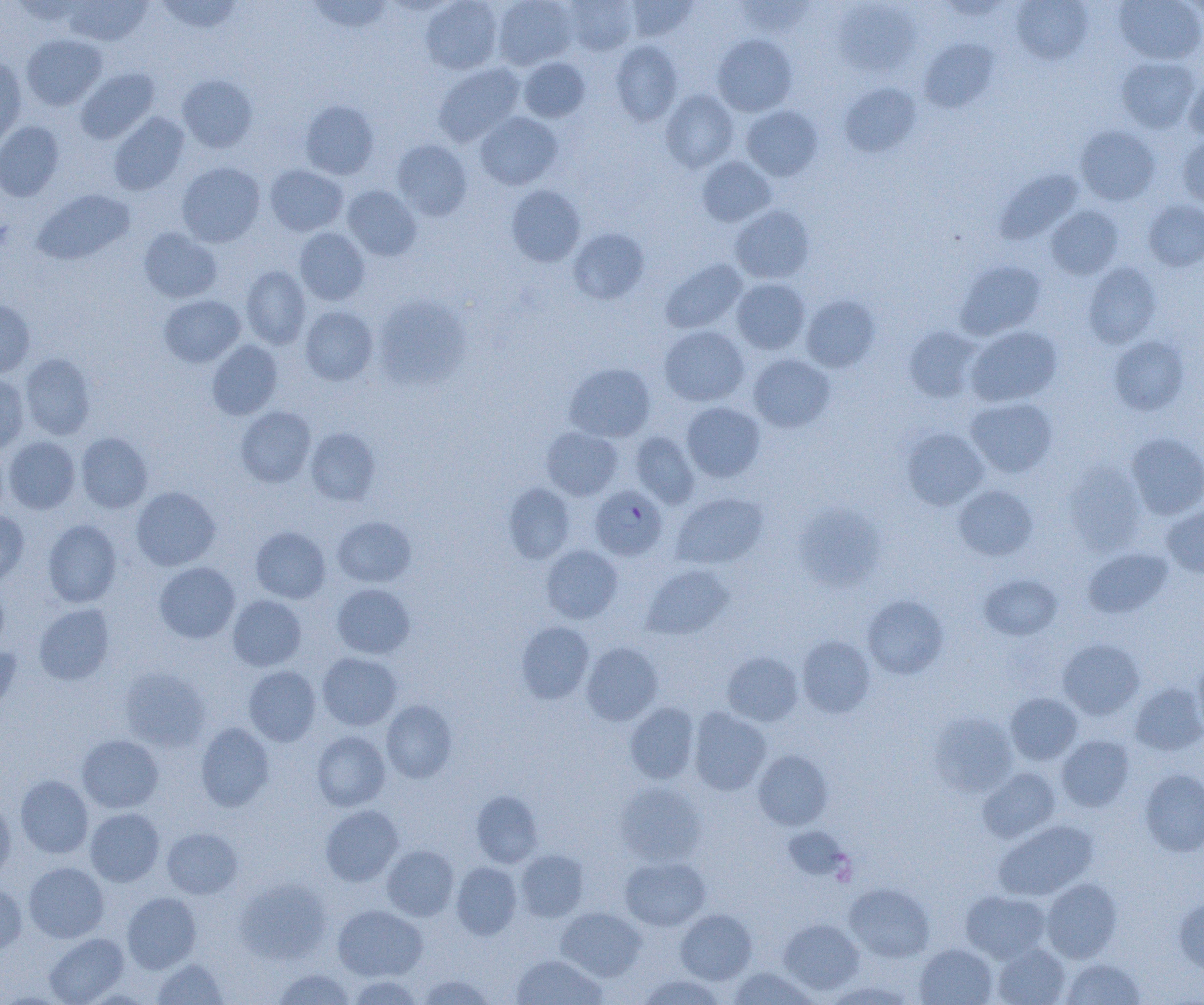
Summary:
  - Coordinate format: approximate bounding boxes as (x1, y1, x2, y2) in pixels
  - Uninfected red blood cell locations: (63, 0, 152, 46), (157, 0, 242, 33), (308, 0, 393, 33), (421, 0, 502, 74), (493, 0, 578, 70), (625, 0, 697, 42), (1011, 0, 1093, 65), (1114, 0, 1204, 64), (566, 1, 637, 55), (735, 1, 816, 36), (835, 2, 920, 76), (21, 34, 107, 110), (712, 35, 797, 117), (920, 39, 998, 112), (610, 40, 683, 125), (0, 55, 26, 149), (518, 57, 590, 122), (1115, 57, 1201, 133), (433, 63, 525, 146), (76, 68, 159, 144), (1184, 72, 1204, 143), (177, 74, 257, 152), (839, 82, 921, 157), (661, 89, 739, 172), (300, 100, 379, 179), (741, 106, 823, 181), (108, 112, 189, 195), (476, 112, 562, 190), (0, 121, 64, 202), (1075, 126, 1160, 205), (1178, 135, 1204, 209), (392, 139, 472, 220), (696, 156, 776, 227), (176, 162, 265, 247), (265, 165, 348, 236), (995, 169, 1084, 244), (343, 185, 422, 260), (506, 185, 585, 267), (33, 189, 135, 265), (1143, 199, 1204, 272), (730, 205, 814, 283), (1046, 206, 1122, 279), (139, 227, 222, 303), (294, 228, 370, 305), (568, 228, 649, 304), (660, 259, 747, 333), (955, 260, 1046, 339), (1083, 262, 1161, 348), (241, 265, 310, 349), (732, 278, 810, 354), (373, 294, 471, 390), (801, 294, 880, 372), (159, 295, 245, 367), (0, 300, 35, 378), (300, 306, 378, 385), (659, 325, 749, 406), (903, 326, 982, 403), (967, 326, 1062, 407), (1107, 335, 1190, 415), (206, 340, 282, 420), (20, 353, 95, 440), (748, 354, 835, 432), (564, 363, 656, 442), (0, 374, 30, 453), (965, 397, 1057, 478), (681, 402, 765, 481), (236, 406, 316, 488), (541, 426, 623, 500), (306, 427, 380, 505), (902, 428, 989, 510), (630, 431, 699, 508), (76, 433, 153, 513), (1126, 433, 1204, 519), (4, 437, 80, 514), (0, 444, 10, 519), (1063, 462, 1146, 554), (504, 482, 576, 564), (953, 485, 1038, 561), (131, 486, 220, 570), (671, 492, 767, 569), (793, 504, 886, 591), (1162, 506, 1204, 578), (0, 509, 29, 587), (333, 516, 416, 587), (43, 519, 122, 607), (250, 526, 330, 603), (541, 545, 622, 623), (1083, 547, 1173, 618), (154, 562, 239, 643), (642, 564, 732, 639), (979, 573, 1061, 640), (0, 581, 9, 656), (332, 584, 415, 659), (228, 595, 306, 671), (862, 595, 949, 678), (34, 603, 114, 685), (516, 621, 594, 704), (797, 635, 875, 717), (1057, 638, 1145, 720), (581, 642, 662, 725), (0, 645, 21, 717), (722, 651, 803, 726), (317, 652, 402, 730), (1192, 658, 1204, 736), (244, 665, 321, 746), (120, 667, 210, 751), (1130, 682, 1204, 755), (1005, 693, 1083, 764), (381, 700, 458, 783), (624, 702, 699, 783), (688, 707, 771, 795), (929, 712, 1018, 796), (196, 722, 274, 811), (312, 731, 390, 811), (77, 734, 162, 812), (1056, 734, 1135, 812), (753, 750, 832, 830), (979, 768, 1060, 843), (1139, 769, 1204, 856), (16, 775, 93, 858), (614, 781, 707, 866), (471, 789, 542, 868), (0, 799, 15, 882), (320, 804, 404, 886), (86, 808, 164, 886), (993, 819, 1097, 901), (784, 826, 849, 880), (162, 827, 242, 898), (382, 845, 459, 920), (516, 849, 589, 922), (620, 856, 710, 930), (24, 862, 109, 943), (451, 862, 522, 939), (1041, 878, 1122, 962), (235, 879, 332, 963), (845, 883, 935, 962), (0, 884, 27, 955), (961, 891, 1051, 963), (122, 892, 201, 972), (1174, 895, 1204, 975), (333, 904, 427, 981), (556, 907, 646, 981), (675, 908, 756, 984), (779, 919, 864, 994), (45, 933, 128, 1004), (914, 943, 997, 1005), (993, 943, 1070, 1005), (512, 954, 606, 1005), (153, 958, 227, 1004), (1060, 958, 1145, 1004), (728, 967, 817, 1004), (271, 968, 356, 1004), (417, 974, 496, 1005), (637, 974, 726, 1004), (346, 976, 423, 1004), (824, 980, 915, 1005)
  - Plasmodium falciparum-infected red blood cell locations: (590, 485, 667, 560)
  - Slide-level diagnosis: Plasmodium falciparum
  - Image size: 1204×1005 pixels
  - Field of view: one of a larger specimen
  - Magnification: 1000x
  - Preparation: thin blood film
  - Modality: optical microscopy